Assess this cell for malaria.
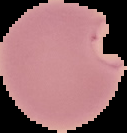
It is parasitized.

The area outside the segmented cell region is set to black. Image is 127×133 pixels. From a thin blood film.